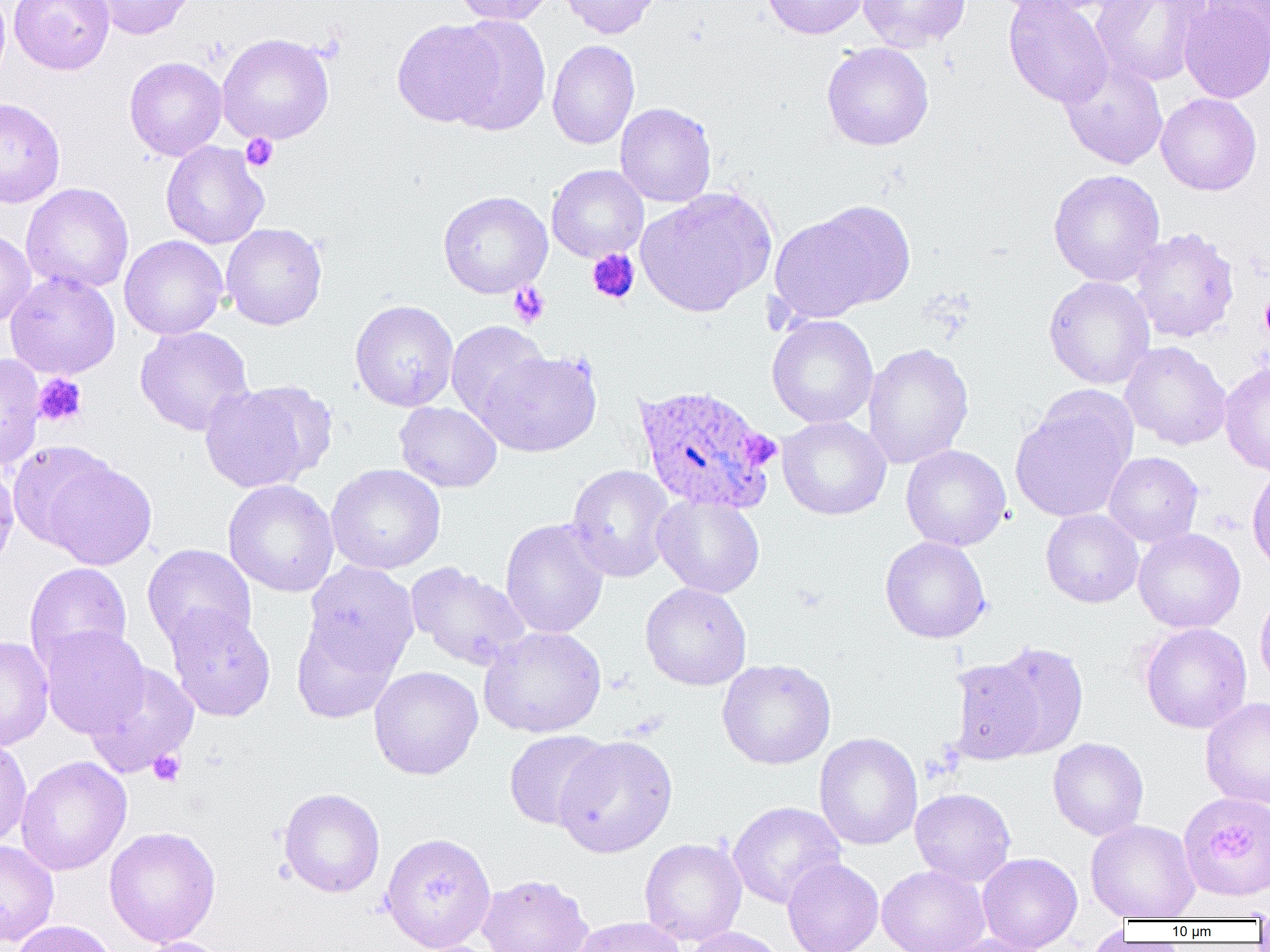

Approximate bounding boxes as (x1, y1, x2, y2) in pixels. Uninfected red blood cell locations: (9, 0, 114, 75), (88, 0, 198, 40), (451, 0, 556, 25), (556, 0, 662, 40), (761, 0, 869, 39), (858, 0, 971, 52), (988, 0, 1118, 17), (1003, 0, 1114, 108), (1091, 0, 1210, 87), (1179, 0, 1270, 104), (1201, 0, 1270, 48), (445, 16, 551, 135), (392, 19, 505, 128), (217, 33, 335, 145), (547, 39, 640, 149), (821, 42, 934, 150), (124, 56, 228, 161), (1059, 56, 1168, 170), (1156, 93, 1262, 195), (0, 97, 65, 208), (615, 102, 716, 207), (161, 140, 269, 249), (546, 164, 648, 262), (1048, 169, 1165, 287), (21, 183, 134, 294), (635, 187, 777, 317), (438, 190, 552, 298), (772, 202, 913, 319), (221, 222, 327, 330), (1130, 227, 1239, 343), (0, 230, 36, 328), (120, 235, 228, 339), (5, 272, 121, 379), (1043, 275, 1155, 389), (350, 300, 458, 411), (767, 315, 878, 428), (446, 320, 552, 426), (134, 325, 254, 436), (1120, 341, 1231, 451), (863, 343, 974, 470), (478, 350, 602, 457), (0, 353, 45, 470), (1219, 361, 1270, 476), (199, 381, 331, 494), (1010, 391, 1137, 522), (394, 401, 502, 493), (777, 415, 891, 520), (7, 441, 114, 549), (900, 444, 1011, 551), (1103, 451, 1203, 547), (42, 458, 157, 570), (0, 460, 20, 569), (325, 463, 446, 574), (566, 464, 677, 582), (1247, 465, 1270, 575), (223, 479, 339, 597), (652, 493, 765, 598), (1041, 509, 1143, 608), (500, 518, 610, 639), (1133, 528, 1245, 633), (880, 536, 991, 643), (142, 544, 257, 652), (25, 562, 132, 670), (303, 562, 420, 674), (406, 562, 530, 671), (640, 582, 752, 690), (1255, 587, 1270, 693), (165, 605, 276, 721), (291, 618, 400, 723), (1140, 622, 1252, 734), (39, 625, 150, 738), (478, 626, 607, 738), (0, 636, 54, 750), (973, 639, 1090, 761), (717, 659, 836, 769), (84, 661, 199, 778), (369, 665, 483, 780), (1200, 697, 1270, 809), (504, 729, 612, 830), (814, 733, 923, 850), (553, 735, 678, 858), (0, 737, 32, 848), (1048, 737, 1148, 841), (16, 756, 132, 875), (279, 788, 385, 898), (910, 788, 1016, 887), (727, 801, 846, 909), (1085, 819, 1200, 921), (103, 826, 221, 948), (381, 832, 496, 952), (639, 838, 747, 945), (0, 840, 59, 947), (977, 852, 1083, 952), (782, 857, 883, 952), (877, 865, 990, 952), (478, 873, 594, 952), (570, 916, 687, 952), (10, 920, 118, 952), (1082, 923, 1131, 952), (683, 926, 787, 952), (932, 934, 1050, 952), (132, 936, 233, 952). Platelet locations: (241, 133, 278, 171), (586, 248, 640, 305), (508, 282, 550, 328), (1259, 291, 1270, 342), (34, 374, 87, 426), (148, 750, 185, 786). Plasmodium ovale-infected red blood cell locations: (632, 383, 782, 515), (1178, 791, 1270, 903). Slide-level diagnosis: Plasmodium ovale. Single field of view. 1000x magnification. Image is 1270×952 pixels. Thin blood smear. Light microscopy.